Classify this cell by malaria status.
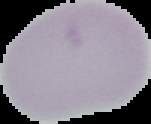

Uninfected.

Image is 151×124 pixels. The area outside the segmented cell region is set to black. From a thin blood film.